Report the malaria status.
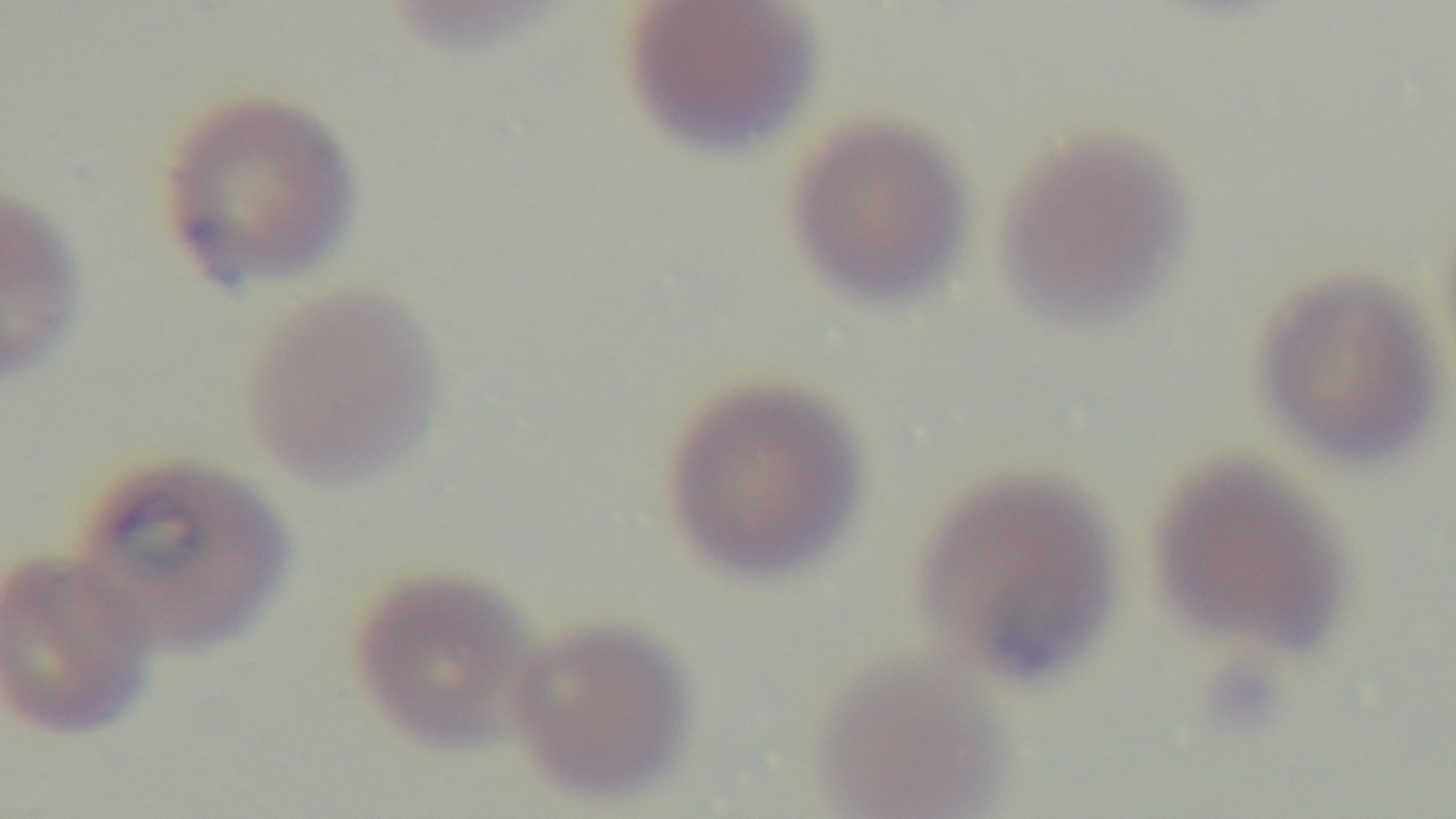
It is infected.

Mounted 4K digital camera. 100x oil-immersion objective. One field from the slide. Preparation: thin. Giemsa-stained. Photomicrograph.